Classify this cell by malaria status.
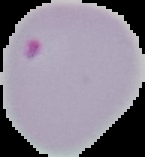

Parasitized.

Summary:
  - Image size: 145×157 pixels
  - Preparation: thin blood film
  - Image type: segmented cell region with the area outside set to black